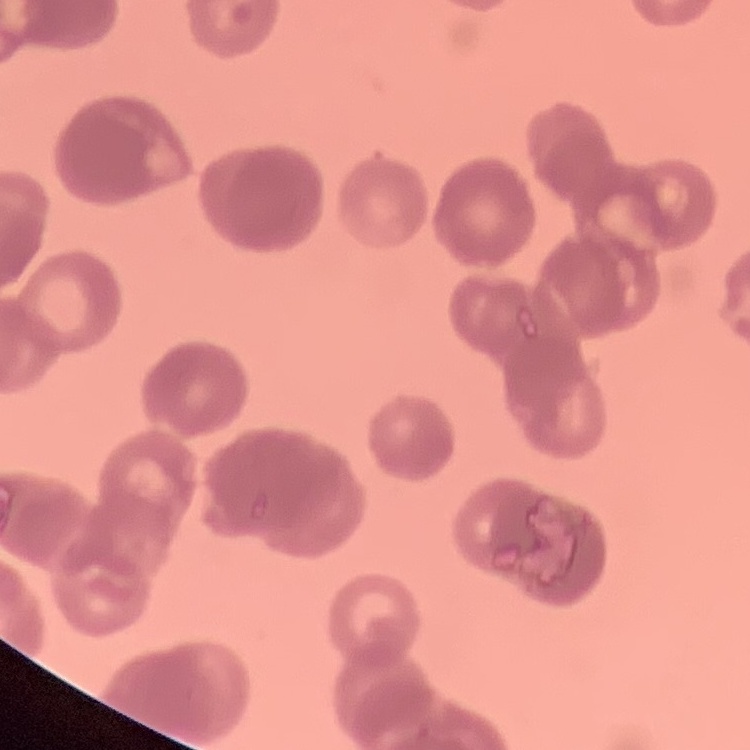

red blood cell morphology = rouleaux formation
image type = one tile cut from a larger photomicrograph
stain = Field's or Giemsa
preparation = thin blood smear